Locate every Trypanosoma brucei.
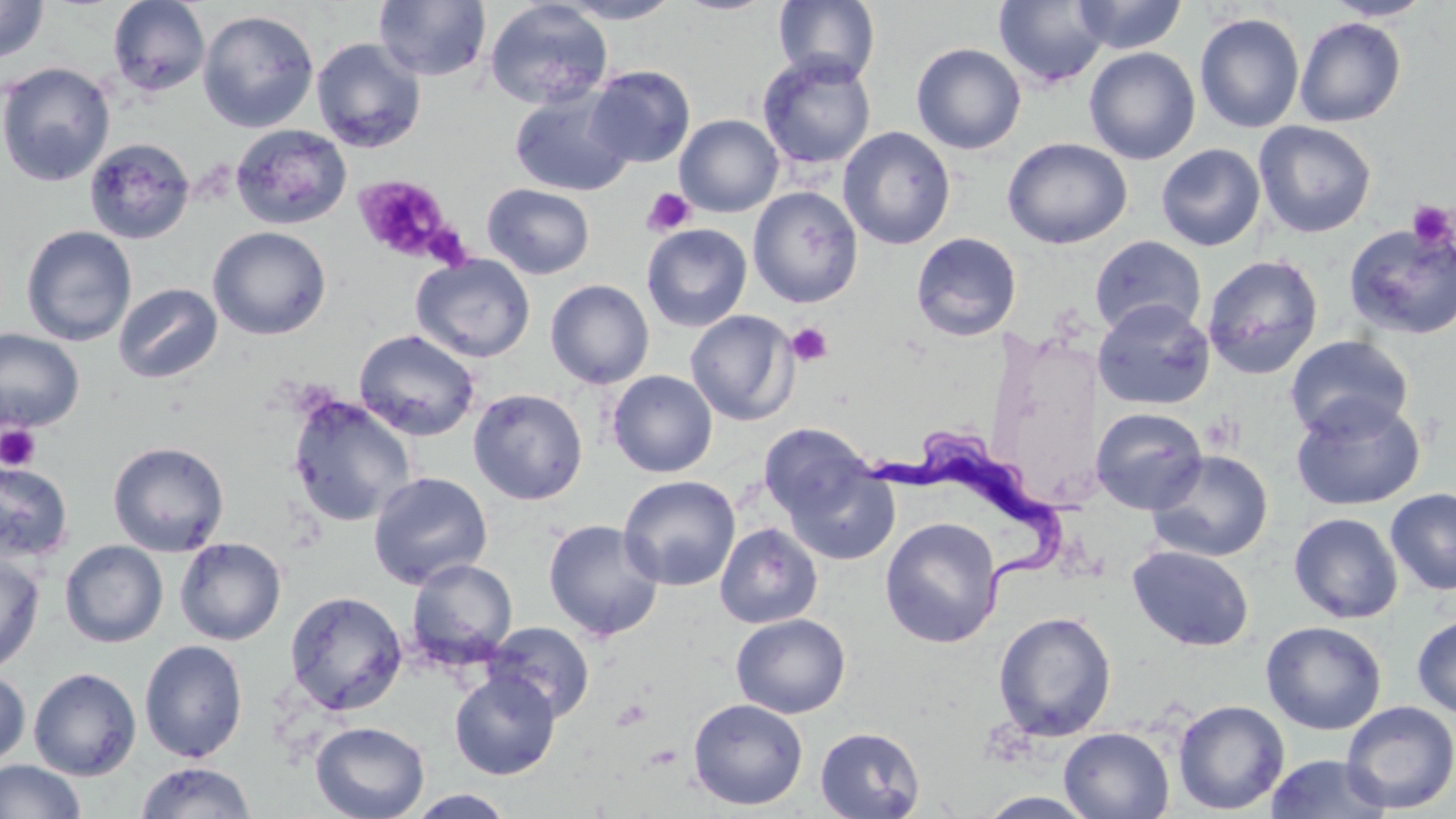
Approximate bounding boxes as (x1,y1)-(x2,y2) corner pairs in pixels.
Trypanosoma brucei: (870,423)-(1071,615).

Uninfected red blood cell locations: (374,0)-(492,82), (554,0)-(684,24), (674,0)-(777,16), (1071,0)-(1188,54), (1321,0)-(1435,21), (0,1)-(50,65), (107,1)-(210,97), (483,1)-(613,110), (773,1)-(881,85), (993,1)-(1111,88), (197,9)-(320,133), (1194,13)-(1305,133), (1295,17)-(1407,127), (310,38)-(427,153), (911,43)-(1027,154), (1084,46)-(1201,165), (757,53)-(876,171), (0,62)-(116,187), (587,65)-(695,168), (509,89)-(635,197), (674,114)-(784,217), (1254,121)-(1377,238), (230,124)-(352,230), (838,126)-(956,250), (84,137)-(196,245), (1002,137)-(1132,249), (1156,144)-(1266,251), (483,183)-(596,279), (748,187)-(863,308), (1343,222)-(1456,341), (641,223)-(752,332), (21,225)-(137,347), (208,226)-(331,340), (910,232)-(1022,342), (1089,235)-(1207,339), (411,254)-(535,363), (1202,254)-(1323,379), (545,279)-(654,389), (113,282)-(223,384), (1093,299)-(1215,410), (685,309)-(799,426), (0,329)-(85,431), (354,329)-(481,442), (1285,335)-(1414,441), (607,370)-(718,478), (468,388)-(588,505), (286,394)-(417,527), (1291,396)-(1426,510), (1090,406)-(1208,514), (758,422)-(874,525), (107,440)-(230,557), (1146,449)-(1274,562), (782,459)-(900,565), (0,460)-(74,563), (368,470)-(493,589), (618,475)-(742,591), (809,487)-(931,629), (1385,488)-(1456,596), (1289,512)-(1403,624), (880,517)-(1003,648), (542,519)-(665,642), (714,522)-(823,629), (174,537)-(286,645), (59,540)-(168,648), (1126,544)-(1254,652), (0,551)-(45,676), (406,558)-(518,667), (285,590)-(407,715), (993,611)-(1117,742), (730,613)-(851,718), (1412,613)-(1456,719), (483,621)-(596,723), (1261,621)-(1387,735), (139,639)-(249,763), (0,667)-(30,770), (29,667)-(141,780), (449,670)-(560,779), (687,698)-(809,810), (1172,699)-(1290,815), (1340,700)-(1456,814), (310,721)-(430,819), (815,727)-(925,818), (1058,727)-(1175,818), (1266,753)-(1392,819), (0,760)-(86,819), (134,761)-(257,818), (407,789)-(516,818), (976,791)-(1100,818). Platelet locations: (352,175)-(454,263), (642,187)-(696,236), (1407,200)-(1455,251), (428,228)-(473,269), (786,322)-(833,367), (1201,414)-(1243,454), (1,424)-(41,472), (611,698)-(652,730). Slide-level diagnosis: Trypanosoma brucei. Single field of view. Captured at 1000x magnification. Thin blood film. Optical microscopy. May-Grünwald-Giemsa stain. Image is 1456×819 pixels.